Identify the parasite.
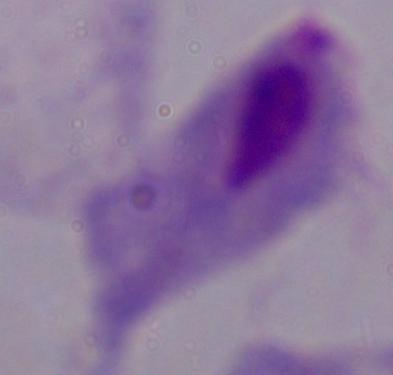

A trichomonad.

Photomicrograph. 1000x magnification.